Locate every blood parasite and identify its species.
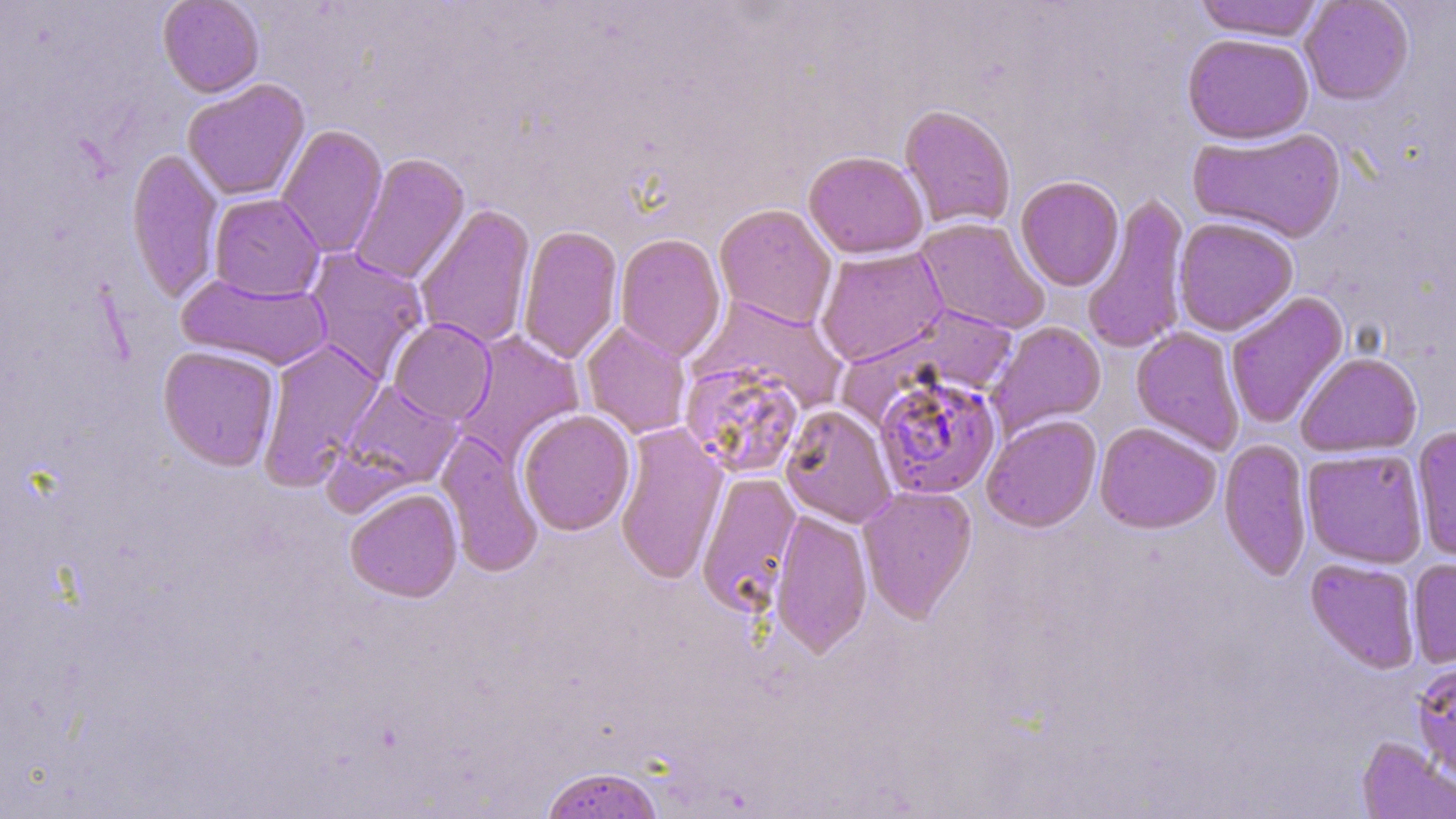

Approximate bounding boxes as (x1, y1, x2, y2) in pixels.
Plasmodium falciparum-infected red blood cells: (872, 373, 1002, 501).
No Plasmodium ovale, Plasmodium malariae, Plasmodium vivax, Babesia divergens, or Trypanosoma brucei observed.

slide-level diagnosis = Plasmodium falciparum
modality = light microscopy
magnification = 1000x
preparation = thin blood smear
image size = 1456×819 pixels
stain = May-Grünwald-Giemsa
field of view = one of a larger specimen
uninfected red blood cell locations = approximate bounding boxes as (x1, y1, x2, y2) in pixels: (157, 0, 264, 97), (1193, 0, 1325, 41), (1300, 0, 1414, 105), (1182, 32, 1315, 144), (182, 79, 310, 201), (899, 104, 1017, 231), (275, 124, 388, 259), (1187, 126, 1346, 244), (126, 147, 224, 304), (803, 150, 928, 259), (349, 153, 470, 285), (1016, 175, 1124, 291), (209, 193, 325, 301), (1081, 194, 1192, 356), (714, 203, 837, 329), (414, 204, 536, 350), (1173, 216, 1299, 336), (914, 217, 1051, 335), (517, 224, 623, 365), (614, 232, 727, 362), (815, 246, 948, 367), (304, 247, 429, 381), (175, 272, 333, 371), (1225, 291, 1348, 429), (691, 295, 847, 416), (842, 304, 1023, 416), (389, 318, 497, 424), (580, 321, 692, 439), (987, 321, 1106, 438), (1131, 326, 1245, 454), (453, 331, 585, 463), (257, 340, 385, 488), (158, 345, 280, 471), (1296, 351, 1423, 457), (680, 359, 807, 480), (339, 380, 463, 493), (780, 404, 897, 528), (517, 409, 636, 536), (981, 414, 1102, 532), (614, 422, 729, 586), (1095, 422, 1222, 534), (1411, 426, 1456, 563), (436, 432, 543, 577), (1219, 438, 1313, 580), (1301, 448, 1428, 568), (696, 471, 802, 615), (858, 484, 978, 623), (345, 487, 463, 602), (770, 508, 873, 659), (1305, 558, 1421, 673), (1408, 559, 1456, 668), (1411, 660, 1456, 781), (1357, 736, 1456, 819), (539, 766, 666, 819)